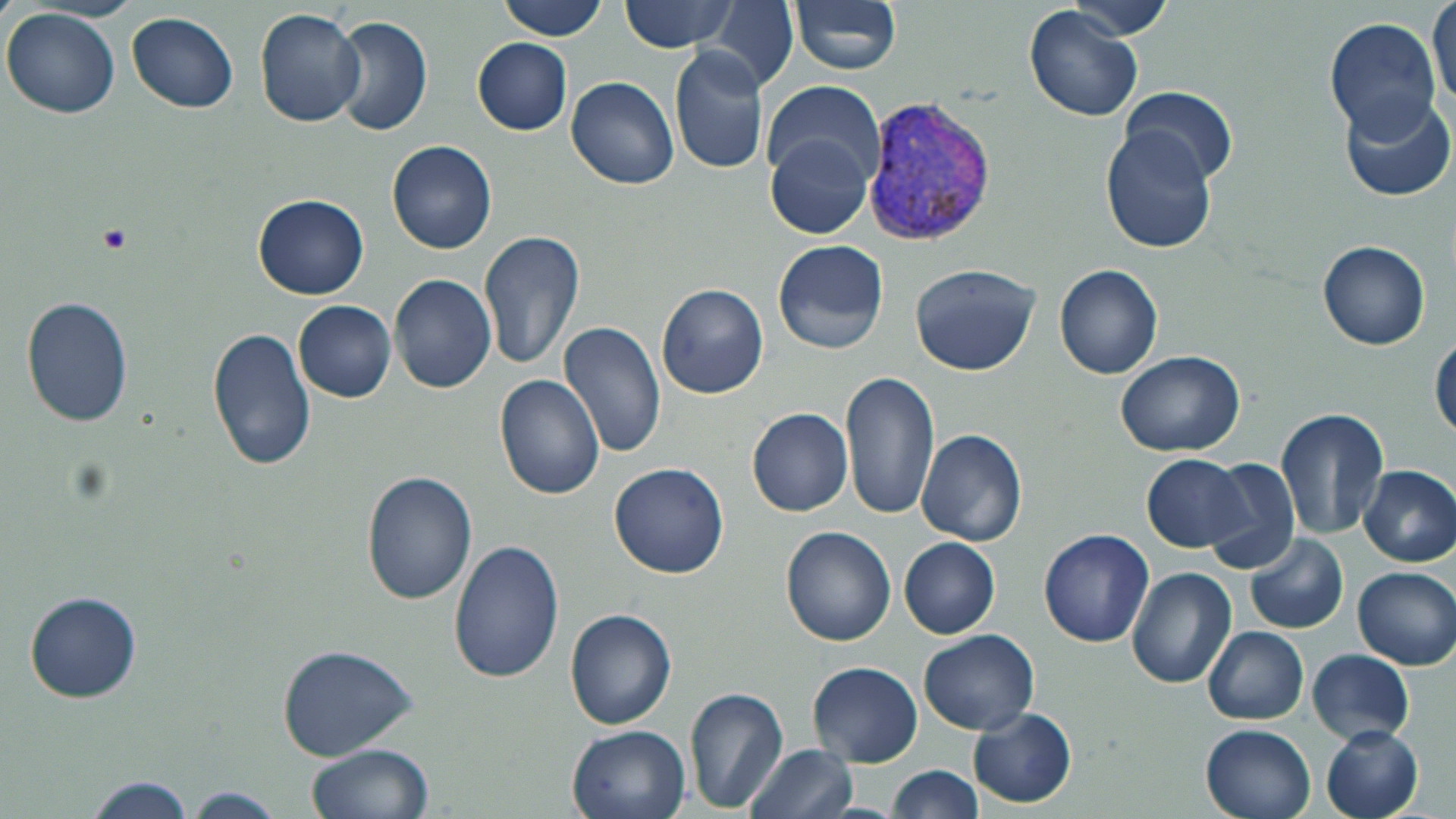

Summary:
  - Coordinate format: approximate bounding boxes as (x1, y1, x2, y2) in pixels
  - Platelet locations: (96, 224, 133, 255)
  - Uninfected red blood cell locations: (496, 0, 609, 41), (619, 0, 739, 53), (789, 0, 902, 75), (1428, 0, 1455, 114), (707, 1, 797, 92), (1063, 2, 1179, 39), (1024, 4, 1144, 122), (1, 7, 120, 119), (253, 8, 368, 128), (128, 11, 239, 113), (330, 16, 433, 137), (1325, 17, 1439, 139), (472, 38, 572, 136), (668, 47, 768, 176), (568, 76, 679, 189), (764, 80, 884, 190), (1118, 87, 1239, 187), (1338, 94, 1454, 202), (1101, 123, 1217, 253), (766, 131, 876, 242), (386, 140, 497, 254), (252, 193, 368, 300), (478, 231, 585, 371), (772, 238, 889, 355), (1317, 241, 1431, 351), (909, 263, 1042, 378), (1054, 264, 1164, 380), (389, 274, 496, 393), (657, 284, 768, 399), (22, 296, 134, 430), (292, 300, 396, 403), (556, 321, 667, 458), (206, 326, 317, 472), (1429, 330, 1456, 440), (1116, 351, 1244, 458), (840, 369, 939, 522), (496, 374, 605, 500), (747, 407, 853, 517), (1276, 409, 1390, 543), (916, 429, 1028, 548), (1141, 455, 1252, 553), (1200, 457, 1300, 575), (608, 462, 730, 580), (1357, 465, 1456, 567), (359, 470, 479, 606), (780, 524, 896, 646), (1039, 528, 1155, 647), (1244, 532, 1349, 635), (899, 537, 1000, 639), (447, 538, 566, 685), (1352, 566, 1456, 670), (1126, 567, 1237, 688), (24, 590, 141, 703), (565, 606, 678, 729), (1204, 625, 1308, 725), (917, 630, 1039, 735), (276, 643, 419, 761), (1306, 650, 1414, 744), (807, 661, 925, 766), (683, 686, 789, 814), (969, 707, 1077, 809), (566, 723, 693, 819), (1199, 723, 1316, 819), (1320, 724, 1423, 819), (304, 744, 435, 819), (743, 744, 858, 819), (884, 764, 981, 819), (83, 776, 196, 818), (178, 787, 293, 817)
  - Plasmodium vivax-infected red blood cell locations: (862, 96, 998, 248)
  - Slide-level diagnosis: Plasmodium vivax
  - Field of view: single
  - Stain: May-Grünwald-Giemsa
  - Preparation: thin blood smear
  - Image size: 1456×819 pixels
  - Modality: light microscopy
  - Magnification: 1000x